Assess this cell for malaria.
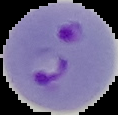
Parasitized.

{
  "image_type": "cell region segmented out of the field of view; surrounding area masked to black",
  "preparation": "thin blood smear",
  "image_size": "118×115 pixels"
}